Report the malaria status of this cell.
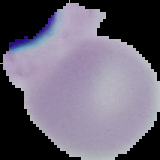

It is uninfected.

Summary:
  - Image size: 160×160 pixels
  - Preparation: thin blood film
  - Image type: segmented cell region with the area outside set to black